Outline each blood parasite and name the species.
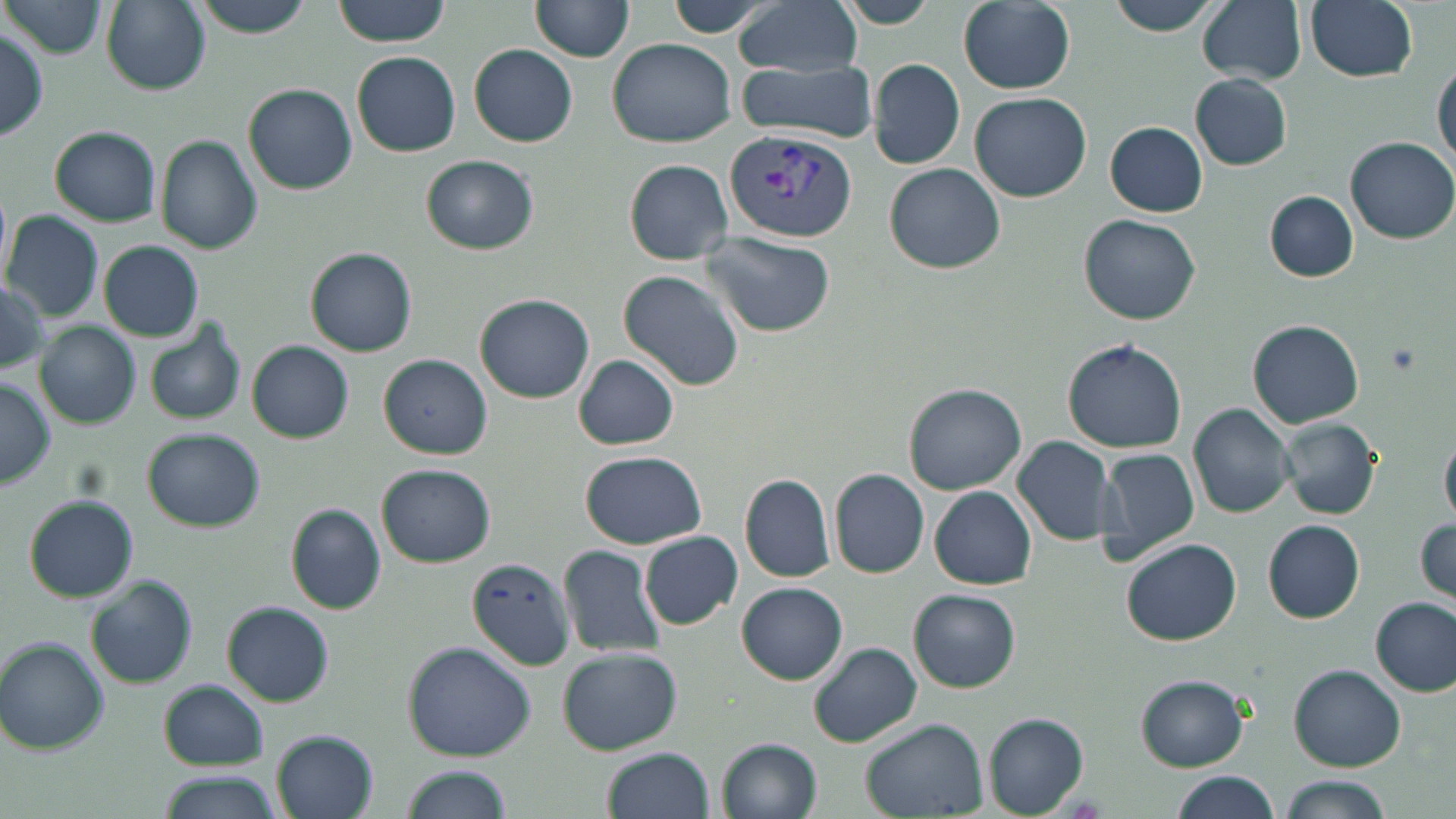
Approximate bounding boxes as (x1,y1)-(x2,y2) corner pairs in pixels.
Plasmodium vivax-infected red blood cells: (725,126)-(857,241).
No Plasmodium falciparum, Plasmodium ovale, Plasmodium malariae, Babesia divergens, or Trypanosoma brucei observed.

Summary:
  - Platelet locations: (1383,342)-(1422,375)
  - Uninfected red blood cell locations: (332,0)-(452,46), (530,0)-(633,63), (733,0)-(861,75), (1103,0)-(1222,36), (1198,0)-(1307,84), (1303,0)-(1418,83), (4,1)-(108,60), (100,1)-(209,94), (186,1)-(319,35), (838,1)-(937,29), (958,1)-(1076,94), (670,2)-(769,39), (0,27)-(50,141), (605,36)-(735,147), (469,43)-(579,146), (352,52)-(462,157), (1432,55)-(1455,171), (868,58)-(965,169), (735,59)-(880,144), (1191,74)-(1294,170), (245,84)-(357,195), (970,91)-(1092,202), (1106,122)-(1207,216), (50,125)-(162,227), (157,135)-(262,255), (1347,137)-(1456,244), (421,154)-(538,253), (624,159)-(732,264), (885,163)-(1005,275), (1264,191)-(1359,281), (4,211)-(103,323), (1078,215)-(1201,325), (699,228)-(835,338), (98,240)-(204,342), (306,247)-(418,356), (619,271)-(745,391), (0,279)-(49,374), (477,294)-(594,401), (1248,319)-(1365,428), (36,322)-(140,430), (145,322)-(246,426), (1062,339)-(1187,453), (247,341)-(354,442), (572,353)-(680,451), (379,354)-(492,459), (0,379)-(55,488), (904,384)-(1027,496), (1189,402)-(1298,518), (1280,417)-(1381,520), (142,428)-(264,532), (1442,429)-(1456,529), (1013,436)-(1120,548), (1096,446)-(1201,564), (580,450)-(709,546), (376,463)-(495,566), (829,469)-(930,578), (741,475)-(834,583), (931,487)-(1036,588), (23,495)-(138,602), (287,504)-(387,615), (1415,517)-(1454,608), (1263,519)-(1366,621), (642,531)-(741,630), (1121,539)-(1242,646), (559,545)-(666,658), (467,557)-(573,669), (86,577)-(197,689), (737,582)-(849,684), (909,588)-(1020,692), (1372,598)-(1454,695), (223,601)-(334,706), (2,639)-(110,753), (402,641)-(536,762), (809,642)-(923,749), (556,647)-(681,755), (1290,664)-(1404,770), (1137,675)-(1250,771), (160,680)-(267,770), (985,714)-(1090,817), (861,719)-(990,818), (273,731)-(381,819), (716,737)-(822,819), (604,748)-(714,819), (399,763)-(510,819), (157,770)-(282,819), (1168,773)-(1281,819), (1278,776)-(1393,819)
  - Slide-level diagnosis: Plasmodium vivax
  - Modality: optical microscopy
  - Image size: 1456×819 pixels
  - Field of view: single
  - Preparation: thin blood smear
  - Magnification: 1000x
  - Stain: May-Grünwald-Giemsa